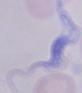

A trypanosome is seen. Micrograph. 1000x magnification.